Give the extent of all Plasmodium falciparum-infected red blood cells.
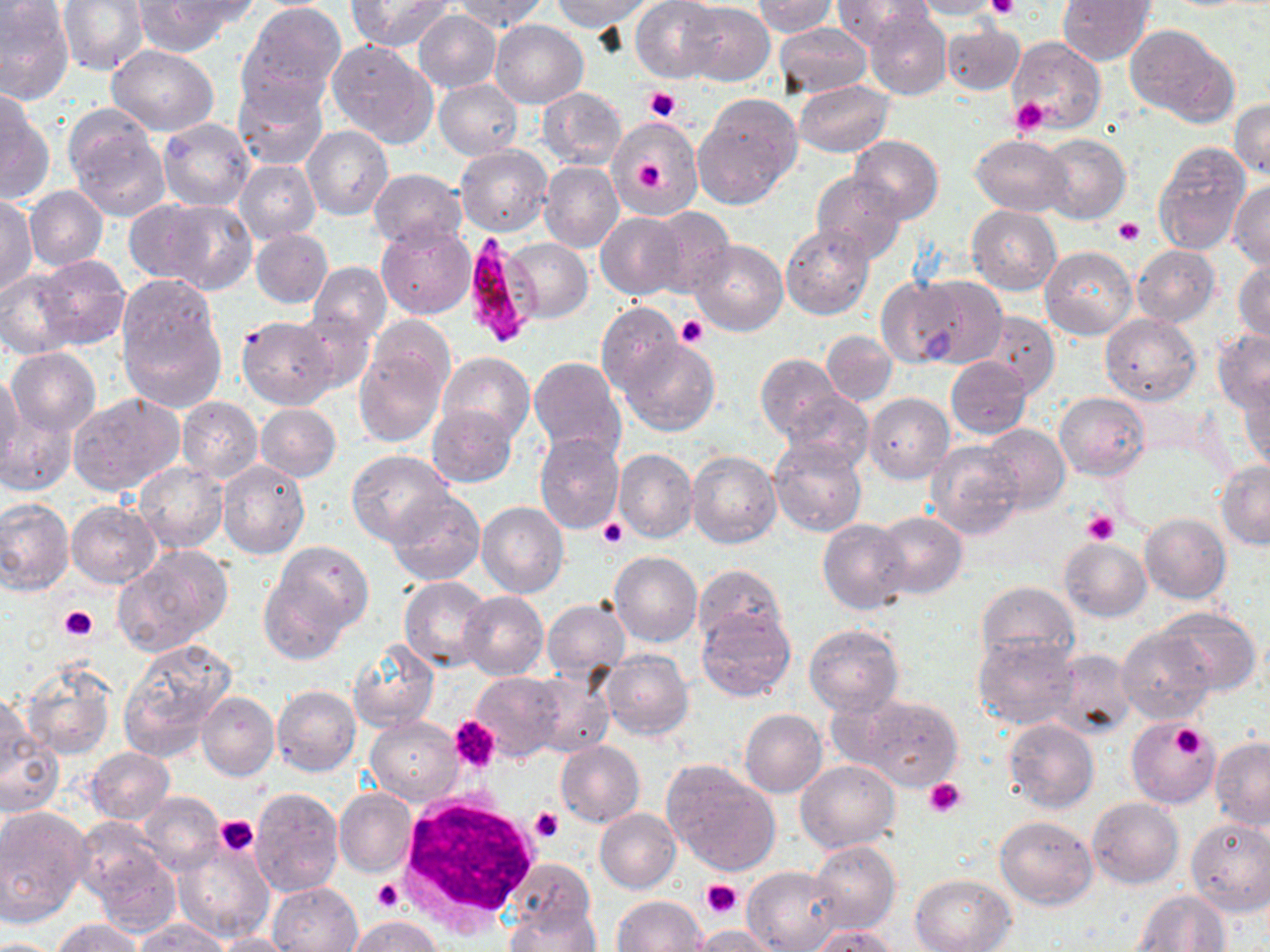
Approximate bounding boxes as [x1, y1, x2, y2] in pixels.
Plasmodium falciparum-infected red blood cells: [462, 233, 537, 347].

slide-level diagnosis = Plasmodium falciparum
field of view = single
preparation = thin blood film
image size = 1270×952 pixels
magnification = 1000x
uninfected red blood cell locations = approximate bounding boxes as [x1, y1, x2, y2] in pixels: [59, 0, 148, 74], [167, 0, 262, 32], [347, 0, 454, 50], [451, 0, 547, 32], [550, 0, 648, 29], [756, 0, 835, 37], [834, 0, 933, 47], [1057, 0, 1155, 65], [128, 1, 232, 55], [631, 1, 723, 82], [909, 1, 1007, 20], [0, 2, 74, 107], [679, 3, 774, 85], [238, 4, 346, 111], [865, 7, 952, 100], [414, 10, 501, 92], [424, 11, 512, 159], [490, 19, 587, 106], [942, 21, 1025, 95], [773, 23, 871, 100], [1124, 24, 1237, 125], [1006, 36, 1106, 133], [327, 38, 438, 149], [108, 44, 219, 135], [435, 79, 523, 160], [442, 80, 531, 236], [793, 81, 894, 157], [234, 82, 327, 171], [536, 88, 627, 169], [0, 90, 51, 205], [693, 93, 801, 207], [1231, 98, 1270, 180], [67, 114, 170, 220], [608, 117, 703, 217], [157, 118, 255, 210], [302, 125, 393, 220], [973, 134, 1073, 216], [1038, 134, 1130, 224], [850, 135, 943, 224], [1153, 142, 1251, 254], [455, 145, 552, 236], [234, 161, 321, 244], [539, 161, 623, 253], [369, 168, 467, 250], [811, 172, 907, 262], [1229, 181, 1269, 270], [25, 186, 107, 270], [1, 193, 38, 299], [123, 197, 220, 284], [153, 200, 258, 294], [966, 205, 1061, 294], [647, 206, 736, 296], [596, 212, 688, 299], [375, 223, 476, 320], [780, 224, 874, 319], [250, 228, 332, 308], [503, 238, 592, 323], [688, 240, 788, 336], [1132, 243, 1219, 327], [1039, 245, 1136, 338], [35, 256, 129, 348], [1234, 258, 1270, 346], [308, 261, 391, 343], [0, 270, 81, 358], [915, 275, 1007, 368], [877, 276, 967, 367], [117, 277, 226, 409], [596, 303, 681, 393], [294, 310, 375, 397], [978, 311, 1058, 396], [1100, 312, 1202, 406], [367, 314, 456, 395], [237, 315, 337, 409], [1211, 330, 1270, 414], [822, 331, 896, 405], [621, 339, 720, 436], [354, 340, 449, 447], [7, 348, 100, 436], [437, 352, 534, 443], [755, 354, 842, 440], [946, 356, 1031, 438], [528, 357, 626, 458], [0, 370, 23, 477], [1240, 381, 1270, 475], [68, 391, 183, 494], [782, 391, 873, 471], [1055, 392, 1150, 480], [865, 393, 954, 483], [177, 397, 263, 483], [255, 404, 340, 481], [427, 404, 519, 487], [1, 408, 76, 497], [980, 422, 1069, 513], [534, 432, 624, 533], [770, 439, 867, 537], [927, 439, 1024, 538], [613, 448, 697, 544], [347, 450, 454, 546], [687, 450, 782, 548], [217, 460, 310, 560], [1216, 461, 1270, 549], [134, 462, 228, 552], [385, 489, 486, 585], [0, 497, 74, 596], [67, 500, 161, 587], [477, 502, 569, 598], [874, 511, 967, 600], [1139, 513, 1230, 603], [818, 519, 912, 614], [1059, 538, 1151, 621], [270, 539, 373, 635], [114, 547, 232, 654], [609, 550, 703, 647], [693, 564, 787, 648], [260, 570, 351, 664], [398, 576, 493, 670], [975, 580, 1078, 671], [459, 592, 549, 680], [542, 598, 630, 686], [696, 607, 796, 703], [1155, 607, 1261, 696], [804, 623, 903, 716], [1117, 627, 1215, 724], [972, 631, 1079, 728], [119, 639, 237, 760], [348, 641, 438, 732], [1049, 648, 1136, 740], [600, 649, 692, 739], [19, 659, 117, 760], [472, 672, 566, 761], [524, 674, 614, 757], [0, 685, 38, 792], [272, 686, 361, 775], [197, 690, 279, 781], [853, 693, 963, 788], [739, 708, 827, 797], [366, 716, 463, 804], [1004, 718, 1099, 813], [1126, 719, 1218, 808], [0, 721, 64, 819], [1209, 737, 1270, 828], [555, 739, 645, 828], [87, 747, 175, 825], [796, 758, 899, 852], [662, 761, 781, 876], [249, 787, 343, 895], [335, 788, 416, 877], [139, 792, 224, 873], [1089, 798, 1184, 888], [0, 806, 91, 925], [595, 809, 681, 892], [995, 814, 1099, 909], [1185, 817, 1270, 916], [174, 839, 274, 942], [808, 840, 900, 932], [83, 842, 180, 938], [508, 858, 594, 934], [742, 865, 844, 952], [910, 873, 1014, 952], [267, 881, 362, 952], [1134, 890, 1232, 951], [613, 896, 706, 951], [504, 904, 600, 952], [346, 915, 443, 951], [52, 918, 143, 951], [134, 920, 232, 951], [688, 925, 785, 951], [809, 926, 899, 951], [214, 932, 297, 951], [0, 936, 58, 951]
white blood cell locations = approximate bounding boxes as [x1, y1, x2, y2] in pixels: [395, 792, 539, 930]
stain = May-Grünwald-Giemsa
modality = optical microscopy
platelet locations = approximate bounding boxes as [x1, y1, x2, y2] in pixels: [986, 0, 1019, 21], [645, 86, 681, 122], [1010, 97, 1051, 136], [635, 161, 665, 190], [1112, 218, 1145, 246], [678, 315, 709, 347], [1082, 510, 1118, 546], [598, 516, 630, 550], [58, 605, 97, 641], [451, 716, 501, 774], [1148, 723, 1215, 784], [1169, 723, 1207, 759], [924, 779, 966, 817], [532, 806, 563, 842], [214, 816, 258, 856], [372, 878, 404, 913], [700, 879, 742, 918]